Name the parasite shown.
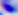

This is Toxoplasma gondii.

{
  "magnification": "400x",
  "modality": "photomicrograph"
}